Comment on the morphology of the erythrocytes.
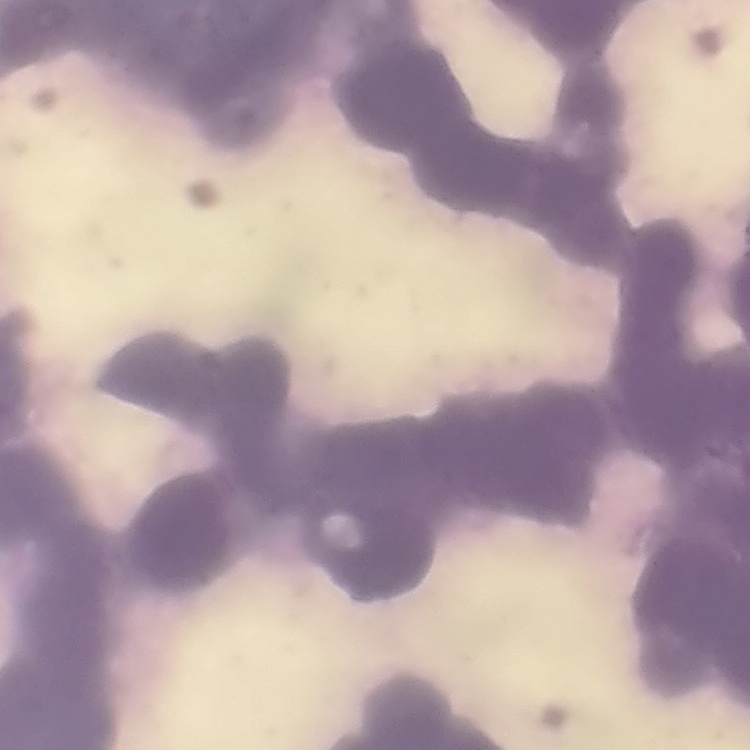

Rouleaux formation.

image type = square crop of a larger photomicrograph
stain = Field's or Giemsa
preparation = thin blood film